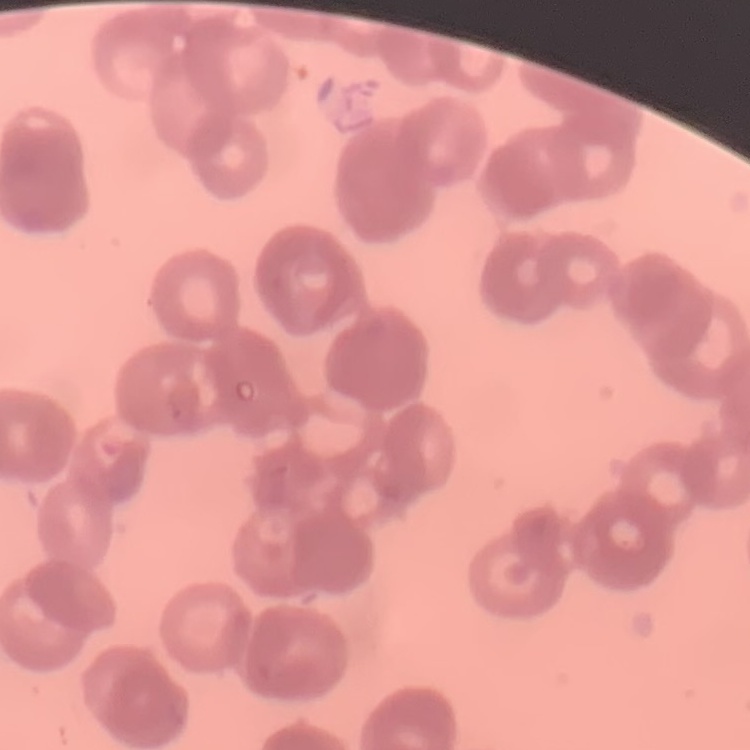
erythrocyte morphology = rouleaux formation
stain = Field's or Giemsa
image type = one tile cut from a larger photomicrograph
preparation = thin blood smear